Assess the morphology of the erythrocytes.
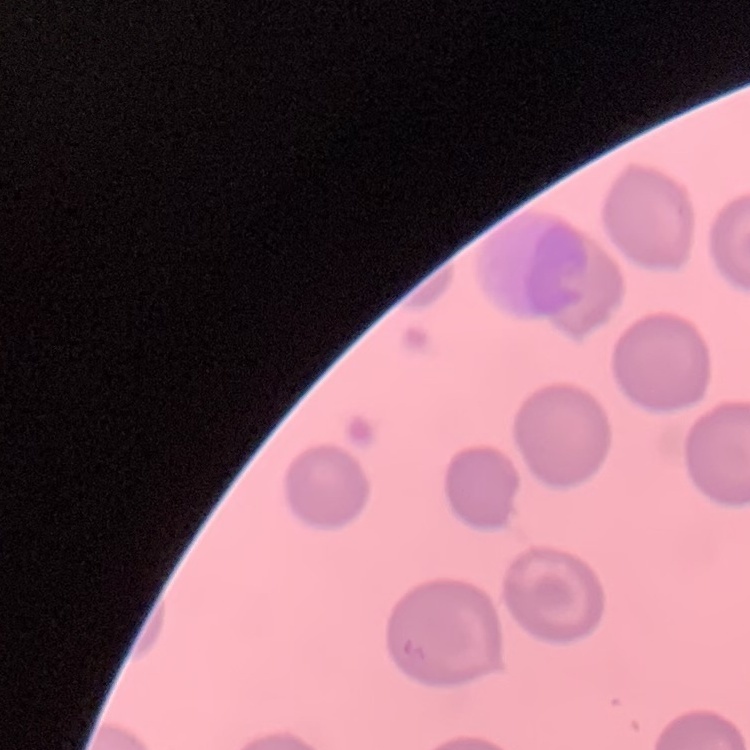
No rouleaux formation.

image_type: square crop of a larger photomicrograph
preparation: thin peripheral smear
stain: Field's or Giemsa